Outline each blood parasite and name the species.
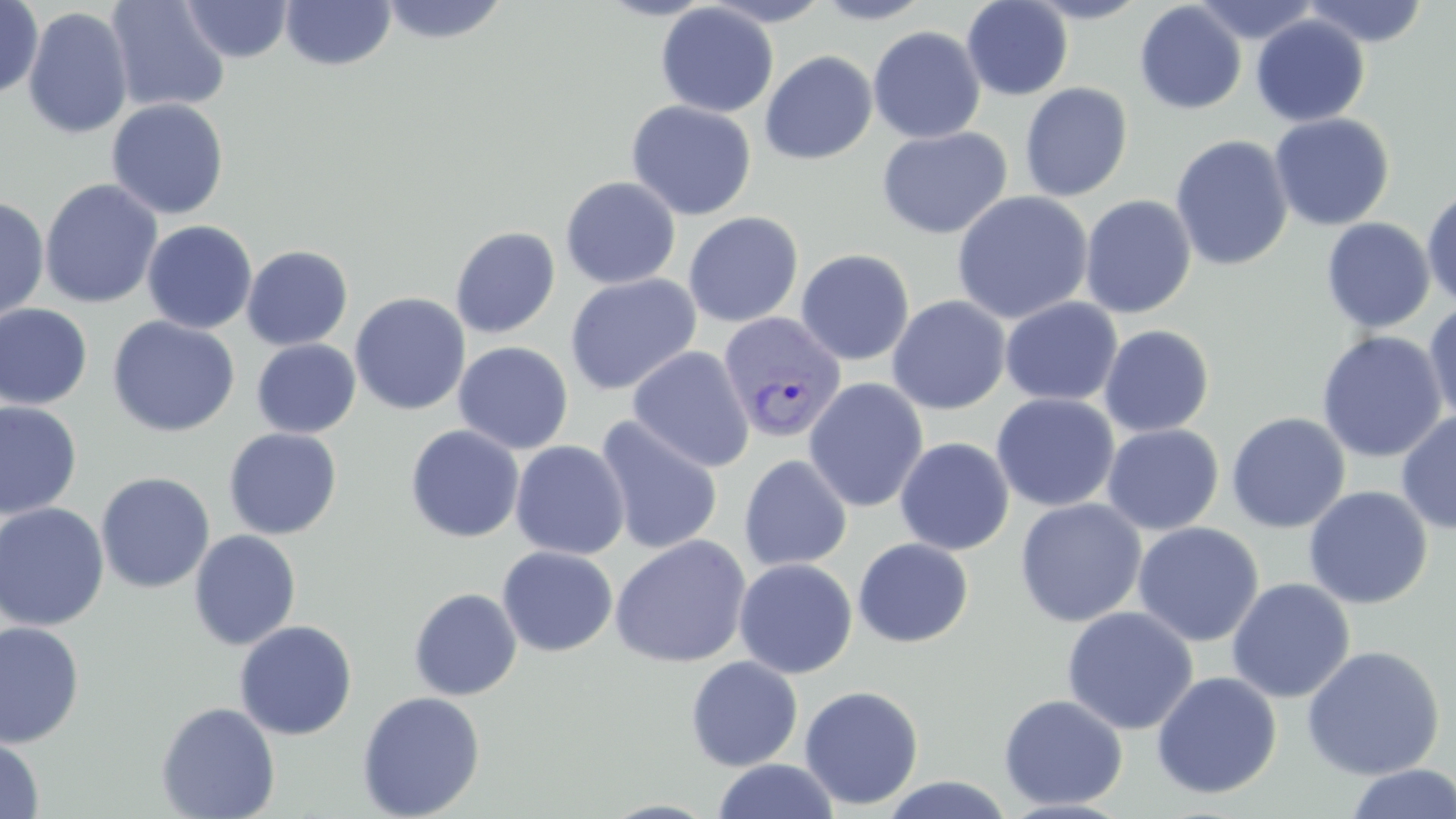

Approximate bounding boxes as named x1/y1/x2/y2 corners in pixels.
Plasmodium vivax-infected red blood cells: (x1=718, y1=312, x2=847, y2=445).
No Plasmodium falciparum, Plasmodium ovale, Plasmodium malariae, Babesia divergens, or Trypanosoma brucei observed.

Summary:
  - Uninfected red blood cell locations: (x1=0, y1=0, x2=43, y2=100), (x1=181, y1=0, x2=293, y2=63), (x1=279, y1=0, x2=397, y2=71), (x1=596, y1=0, x2=718, y2=21), (x1=701, y1=0, x2=835, y2=27), (x1=812, y1=0, x2=934, y2=25), (x1=961, y1=0, x2=1073, y2=100), (x1=1022, y1=0, x2=1153, y2=24), (x1=1300, y1=0, x2=1431, y2=48), (x1=105, y1=1, x2=231, y2=113), (x1=377, y1=1, x2=510, y2=46), (x1=1192, y1=1, x2=1322, y2=44), (x1=655, y1=2, x2=779, y2=118), (x1=1134, y1=2, x2=1247, y2=115), (x1=23, y1=7, x2=134, y2=140), (x1=1250, y1=14, x2=1370, y2=127), (x1=867, y1=25, x2=986, y2=144), (x1=759, y1=50, x2=878, y2=164), (x1=1019, y1=82, x2=1133, y2=202), (x1=106, y1=98, x2=229, y2=220), (x1=626, y1=100, x2=757, y2=220), (x1=1269, y1=113, x2=1394, y2=231), (x1=876, y1=126, x2=1013, y2=240), (x1=1171, y1=135, x2=1293, y2=272), (x1=560, y1=176, x2=681, y2=289), (x1=40, y1=178, x2=163, y2=309), (x1=1422, y1=186, x2=1456, y2=309), (x1=951, y1=190, x2=1093, y2=324), (x1=1080, y1=195, x2=1197, y2=319), (x1=0, y1=196, x2=50, y2=325), (x1=683, y1=211, x2=804, y2=327), (x1=1321, y1=218, x2=1435, y2=334), (x1=141, y1=219, x2=258, y2=335), (x1=450, y1=226, x2=561, y2=339), (x1=241, y1=245, x2=353, y2=350), (x1=795, y1=248, x2=915, y2=366), (x1=565, y1=273, x2=702, y2=396), (x1=350, y1=293, x2=471, y2=415), (x1=887, y1=295, x2=1011, y2=415), (x1=999, y1=297, x2=1123, y2=406), (x1=1423, y1=301, x2=1456, y2=427), (x1=0, y1=303, x2=93, y2=410), (x1=107, y1=315, x2=241, y2=438), (x1=1099, y1=324, x2=1215, y2=437), (x1=1316, y1=331, x2=1448, y2=463), (x1=251, y1=338, x2=361, y2=438), (x1=453, y1=341, x2=574, y2=455), (x1=627, y1=346, x2=755, y2=473), (x1=804, y1=378, x2=928, y2=513), (x1=991, y1=393, x2=1120, y2=512), (x1=0, y1=400, x2=82, y2=520), (x1=1396, y1=409, x2=1456, y2=535), (x1=1226, y1=412, x2=1350, y2=533), (x1=594, y1=417, x2=724, y2=556), (x1=1102, y1=423, x2=1224, y2=535), (x1=405, y1=425, x2=525, y2=543), (x1=223, y1=427, x2=342, y2=539), (x1=894, y1=437, x2=1014, y2=556), (x1=509, y1=440, x2=630, y2=560), (x1=738, y1=454, x2=853, y2=571), (x1=96, y1=472, x2=215, y2=594), (x1=1303, y1=486, x2=1433, y2=609), (x1=1014, y1=498, x2=1147, y2=628), (x1=0, y1=502, x2=110, y2=631), (x1=1132, y1=522, x2=1265, y2=647), (x1=188, y1=529, x2=302, y2=651), (x1=610, y1=534, x2=752, y2=668), (x1=853, y1=538, x2=974, y2=647), (x1=497, y1=547, x2=618, y2=656), (x1=734, y1=558, x2=858, y2=679), (x1=1226, y1=578, x2=1355, y2=703), (x1=409, y1=587, x2=522, y2=701), (x1=1061, y1=605, x2=1199, y2=735), (x1=233, y1=620, x2=357, y2=740), (x1=0, y1=622, x2=85, y2=748), (x1=1301, y1=645, x2=1445, y2=781), (x1=685, y1=655, x2=803, y2=772), (x1=1151, y1=671, x2=1282, y2=799), (x1=799, y1=685, x2=924, y2=810), (x1=357, y1=691, x2=485, y2=819), (x1=998, y1=694, x2=1128, y2=811), (x1=155, y1=702, x2=280, y2=819), (x1=0, y1=736, x2=44, y2=818), (x1=713, y1=759, x2=839, y2=818), (x1=1343, y1=764, x2=1456, y2=819), (x1=878, y1=776, x2=1018, y2=818)
  - Slide-level diagnosis: Plasmodium vivax
  - Image size: 1456×819 pixels
  - Modality: optical microscopy
  - Field of view: single
  - Stain: May-Grünwald-Giemsa
  - Magnification: 1000x
  - Preparation: thin blood smear